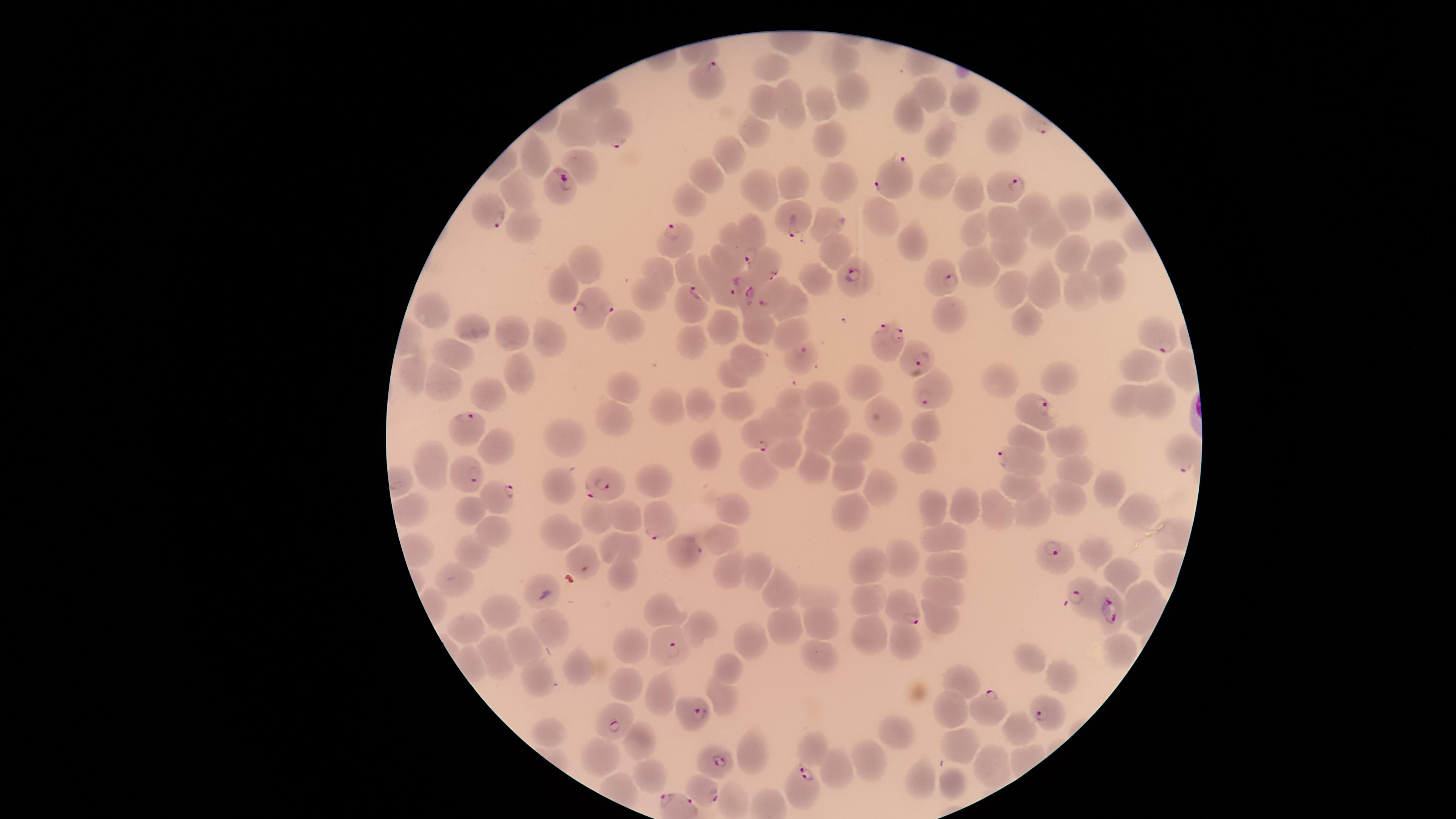

Approximate marker points as {x, y} in pixels.
Summary:
  - Uninfected red blood cells: {842, 59}, {767, 64}, {929, 92}, {850, 94}, {761, 96}, {598, 100}, {969, 100}, {794, 101}, {819, 107}, {909, 120}, {572, 125}, {752, 127}, {1002, 136}, {829, 138}, {935, 138}, {531, 154}, {728, 154}, {580, 159}, {712, 177}, {792, 179}, {937, 185}, {518, 187}, {844, 187}, {761, 189}, {970, 191}, {684, 195}, {1031, 206}, {1106, 208}, {1075, 212}, {880, 218}, {523, 219}, {827, 224}, {1011, 224}, {978, 231}, {1050, 231}, {727, 232}, {911, 239}, {1009, 249}, {833, 251}, {1073, 252}, {1114, 252}, {725, 260}, {583, 264}, {685, 267}, {986, 269}, {661, 272}, {1111, 276}, {814, 278}, {1046, 283}, {563, 285}, {1081, 285}, {1012, 287}, {645, 294}, {798, 305}, {434, 309}, {949, 313}, {1026, 316}, {624, 324}, {475, 325}, {723, 325}, {757, 330}, {791, 333}, {508, 334}, {551, 337}, {694, 340}, {451, 349}, {749, 360}, {1144, 362}, {407, 373}, {729, 376}, {519, 377}, {1000, 377}, {872, 380}, {1061, 380}, {449, 381}, {488, 389}, {624, 392}, {818, 395}, {1121, 400}, {1160, 400}, {793, 403}, {699, 404}, {738, 404}, {671, 408}, {611, 414}, {831, 421}, {790, 424}, {892, 427}, {924, 428}, {1025, 437}, {564, 438}, {822, 439}, {1072, 442}, {502, 446}, {707, 450}, {856, 450}, {788, 451}, {918, 454}, {760, 466}, {818, 470}, {437, 472}, {1070, 472}, {845, 475}, {649, 481}, {877, 485}, {561, 486}, {1110, 486}, {1016, 487}, {1061, 499}, {473, 507}, {931, 507}, {968, 507}, {734, 509}, {994, 510}, {1032, 511}, {852, 512}, {621, 515}, {1139, 516}, {595, 517}, {491, 528}, {558, 532}, {717, 536}, {939, 536}, {627, 541}, {471, 548}, {1094, 551}, {577, 556}, {909, 561}, {940, 564}, {870, 565}, {725, 568}, {616, 569}, {754, 571}, {1121, 575}, {455, 581}, {541, 585}, {943, 587}, {1142, 591}, {777, 592}, {870, 595}, {820, 598}, {665, 606}, {497, 616}, {940, 618}, {553, 622}, {822, 623}, {471, 624}, {784, 624}, {702, 627}, {870, 629}, {753, 639}, {908, 642}, {526, 645}, {634, 650}, {1115, 651}, {494, 655}, {823, 656}, {1027, 662}, {728, 666}, {579, 668}, {537, 677}, {960, 678}, {1058, 678}, {621, 682}, {656, 692}, {720, 692}, {949, 705}, {1021, 725}, {547, 729}, {897, 736}, {636, 740}, {812, 743}, {961, 743}, {752, 745}, {593, 754}, {867, 760}, {990, 764}, {836, 767}, {642, 772}, {921, 779}, {953, 783}
  - Parasitized red blood cells: {705, 77}, {615, 134}, {888, 176}, {1009, 187}, {560, 189}, {486, 210}, {793, 218}, {754, 234}, {669, 239}, {768, 264}, {847, 277}, {944, 278}, {728, 294}, {749, 294}, {693, 298}, {766, 301}, {595, 308}, {886, 335}, {1165, 341}, {805, 354}, {916, 358}, {926, 392}, {1036, 412}, {465, 421}, {756, 436}, {1180, 457}, {1011, 458}, {468, 469}, {609, 485}, {499, 491}, {658, 525}, {686, 547}, {1058, 558}, {1081, 600}, {1109, 610}, {907, 614}, {665, 647}, {988, 711}, {1043, 712}, {696, 713}, {613, 718}, {714, 758}, {807, 784}, {701, 792}
  - Image size: 1456×819 pixels
  - Stain: Giemsa
  - Visible region: circular
  - Preparation: thin smear of blood
  - Species: Plasmodium falciparum
  - Capture: smartphone photograph through the microscope eyepiece
  - Field of view: single
  - Presence: malaria parasites identified